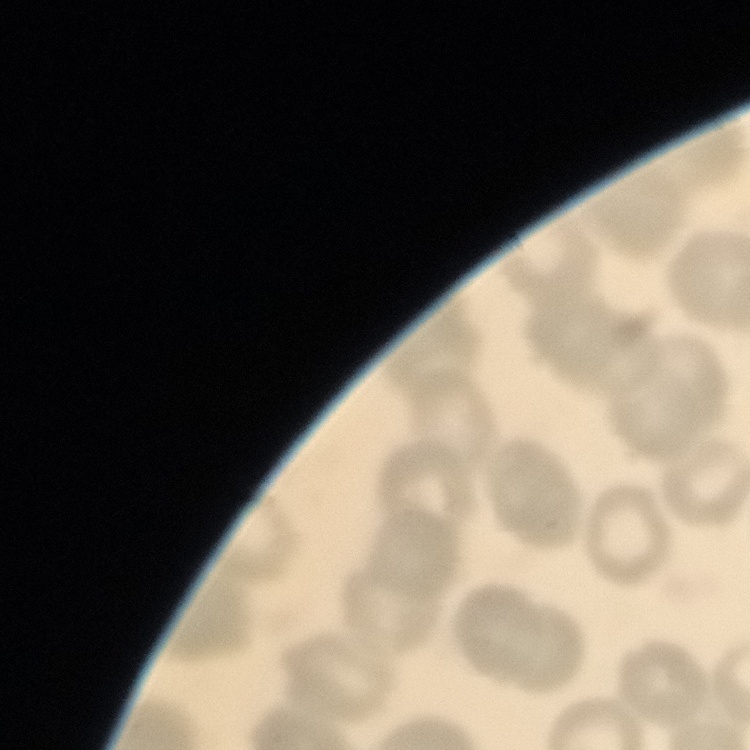

red_blood_cell_morphology: no rouleaux formation
stain: Field's or Giemsa
image_type: one tile cut from a larger photomicrograph
preparation: thin blood film